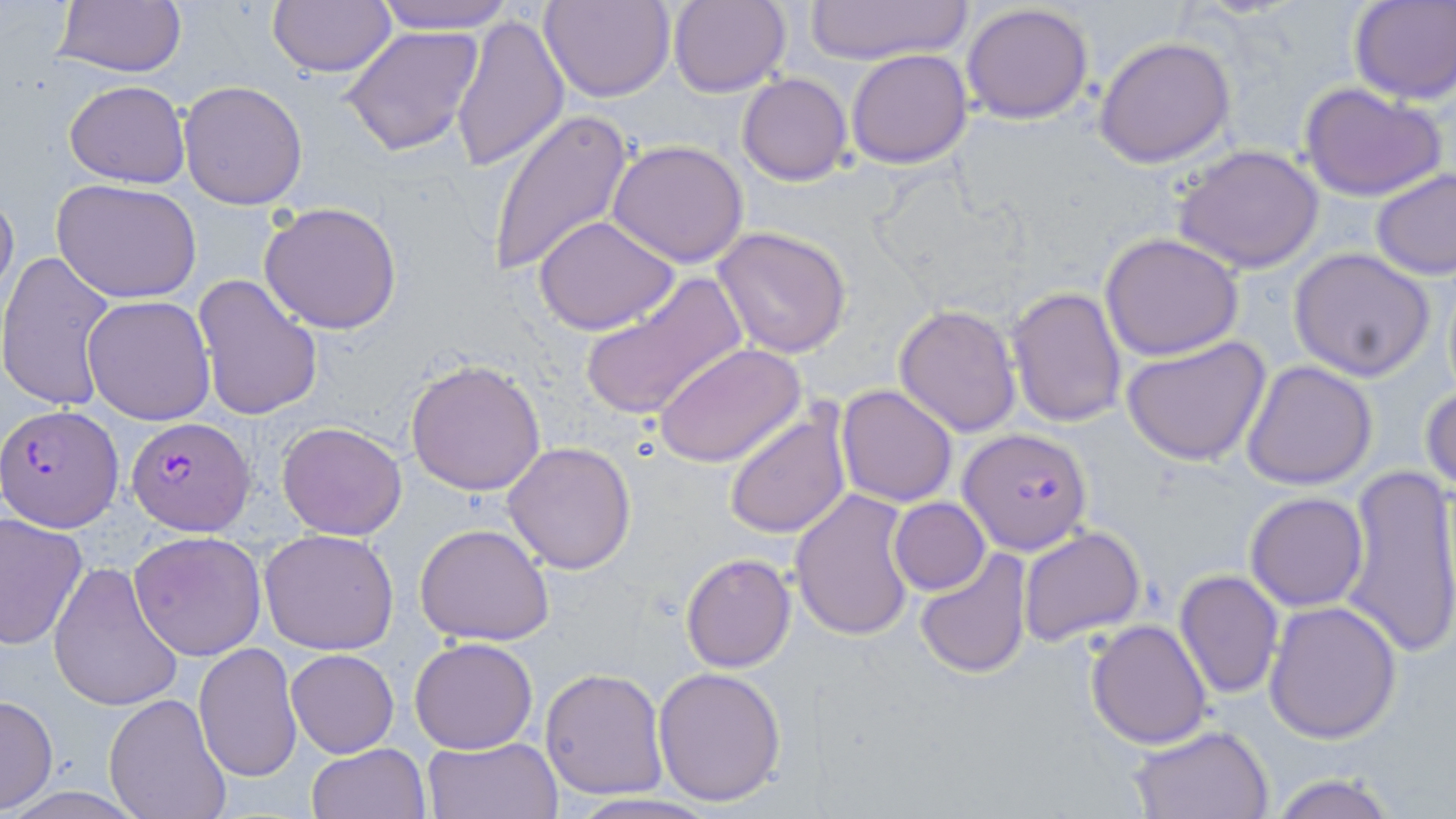
slide_level_diagnosis: Plasmodium falciparum
modality: light microscopy
image_size: 1456×819 pixels
plasmodium_falciparum_infected_red_blood_cell_locations: 'approximate bounding boxes as (x1,y1)-(x2,y2) corner pairs in pixels: (1,402)-(124,529), (128,419)-(258,538), (959,428)-(1090,555)'
stain: May-Grünwald-Giemsa
field_of_view: single
uninfected_red_blood_cell_locations: 'approximate bounding boxes as (x1,y1)-(x2,y2) corner pairs in pixels: (53,0)-(188,80), (267,0)-(398,77), (369,0)-(518,33), (540,0)-(675,102), (668,0)-(791,98), (1349,0)-(1455,105), (809,1)-(969,64), (961,2)-(1094,123), (448,11)-(567,172), (340,24)-(486,157), (1095,36)-(1235,167), (846,49)-(973,168), (737,73)-(853,186), (66,79)-(190,189), (179,81)-(309,210), (1299,81)-(1448,202), (487,109)-(633,277), (607,139)-(751,267), (1174,144)-(1325,274), (1371,167)-(1455,279), (52,178)-(203,305), (0,181)-(18,310), (258,200)-(404,335), (534,216)-(680,334), (712,226)-(855,358), (1100,232)-(1244,360), (1288,248)-(1437,381), (0,250)-(118,412), (193,273)-(325,421), (577,273)-(747,422), (1006,286)-(1128,431), (84,295)-(217,427), (893,303)-(1022,436), (1120,335)-(1272,466), (655,342)-(806,468), (404,357)-(547,496), (1241,360)-(1378,490), (1420,382)-(1455,493), (836,384)-(959,506), (724,407)-(851,539), (277,420)-(406,539), (503,440)-(638,575), (1337,464)-(1456,662), (791,488)-(916,640), (1244,492)-(1368,611), (889,498)-(990,595), (0,512)-(90,650), (415,523)-(554,645), (1018,526)-(1146,647), (258,527)-(399,654), (129,530)-(266,660), (916,549)-(1033,677), (680,552)-(795,672), (47,560)-(184,714), (1174,570)-(1284,698), (1264,601)-(1402,744), (1086,620)-(1214,748), (409,638)-(538,754), (193,642)-(302,780), (286,649)-(398,756), (652,666)-(787,805), (539,667)-(668,799), (104,693)-(233,819), (0,694)-(57,812), (1127,722)-(1273,818), (422,736)-(562,819), (306,742)-(432,819), (1264,774)-(1403,819), (563,793)-(724,819)'
preparation: thin blood smear
magnification: 1000x